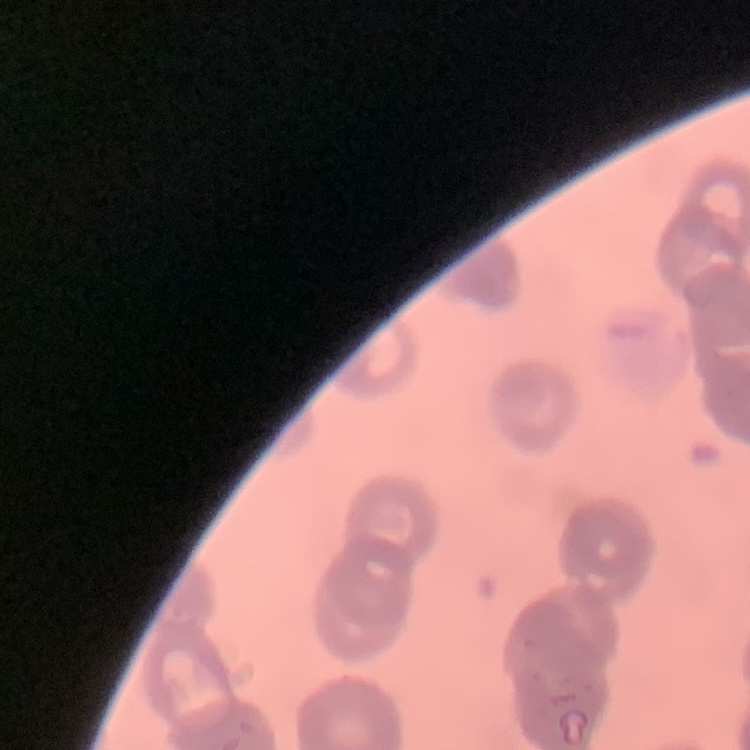

The red blood cells exhibit rouleaux formation. Thin blood smear. Field's or Giemsa stain. Square crop of a larger photomicrograph.